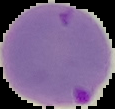

image size = 115×109 pixels
image type = segmented cell region with the area outside set to black
preparation = thin blood film
malaria status = parasitized